Outline each Plasmodium ovale-infected red blood cell.
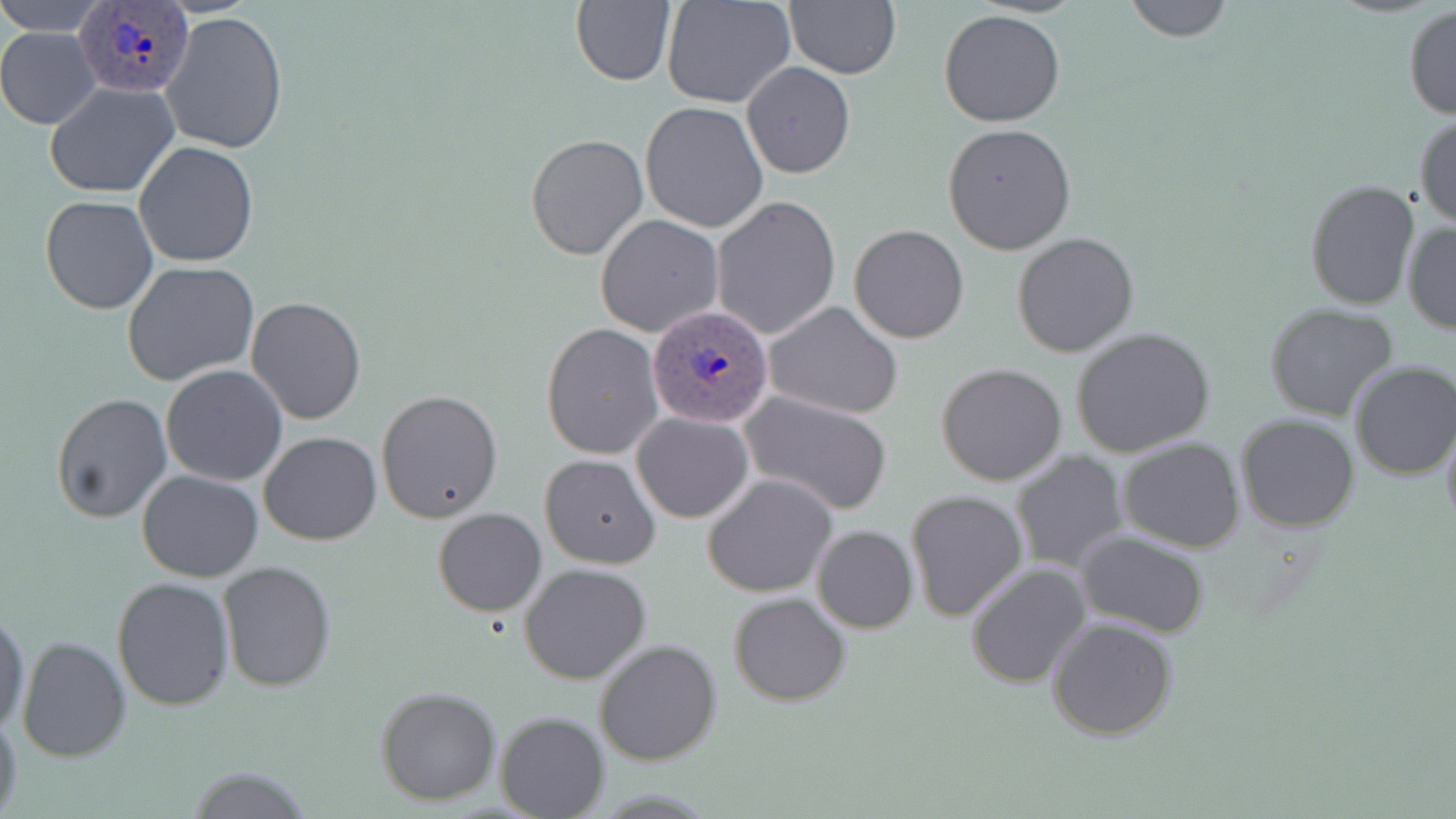

Approximate bounding boxes as [x1, y1, x2, y2] in pixels.
Plasmodium ovale-infected red blood cells: [74, 4, 190, 95], [646, 303, 774, 428].

Summary:
  - Uninfected red blood cell locations: [2, 0, 108, 32], [571, 0, 678, 87], [662, 0, 797, 109], [1120, 0, 1235, 43], [784, 1, 901, 79], [1403, 4, 1456, 120], [939, 9, 1067, 127], [159, 12, 289, 156], [0, 28, 99, 129], [741, 62, 856, 179], [46, 82, 180, 198], [639, 102, 768, 233], [1414, 112, 1456, 229], [942, 122, 1077, 254], [526, 133, 648, 261], [135, 141, 258, 267], [1304, 179, 1421, 311], [40, 195, 159, 315], [710, 197, 841, 340], [595, 215, 725, 338], [1402, 220, 1455, 334], [849, 224, 969, 344], [1012, 231, 1141, 358], [122, 262, 261, 387], [246, 297, 366, 426], [762, 300, 904, 419], [1264, 302, 1402, 423], [541, 324, 663, 460], [1070, 326, 1216, 457], [1347, 361, 1456, 481], [936, 362, 1067, 486], [161, 365, 288, 485], [376, 388, 504, 524], [51, 391, 172, 524], [739, 391, 893, 515], [724, 402, 882, 613], [632, 412, 753, 523], [1235, 414, 1361, 533], [1441, 418, 1456, 536], [259, 430, 382, 545], [1118, 437, 1245, 553], [1010, 450, 1129, 575], [539, 453, 662, 569], [137, 469, 265, 582], [703, 473, 837, 596], [905, 489, 1028, 621], [432, 507, 547, 616], [811, 525, 918, 632], [1075, 531, 1211, 638], [218, 561, 338, 693], [519, 562, 653, 686], [966, 562, 1093, 689], [112, 577, 235, 710], [730, 592, 852, 707], [1, 606, 31, 734], [1046, 616, 1179, 741], [16, 634, 131, 762], [594, 638, 723, 766], [375, 686, 501, 806], [0, 707, 23, 819], [495, 711, 609, 817], [179, 766, 314, 819]
  - Slide-level diagnosis: Plasmodium ovale
  - Magnification: 1000x
  - Stain: May-Grünwald-Giemsa
  - Field of view: single
  - Preparation: thin blood smear
  - Image size: 1456×819 pixels
  - Modality: light microscopy